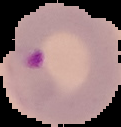
Summary:
  - Malaria status: parasitized
  - Image type: cell region segmented out of the field of view; surrounding area masked to black
  - Preparation: thin blood smear
  - Image size: 121×127 pixels